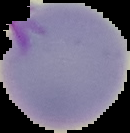

result: Plasmodium parasites identified
image_size: 130×133 pixels
preparation: thin blood film
image_type: segmented cell region on a black background